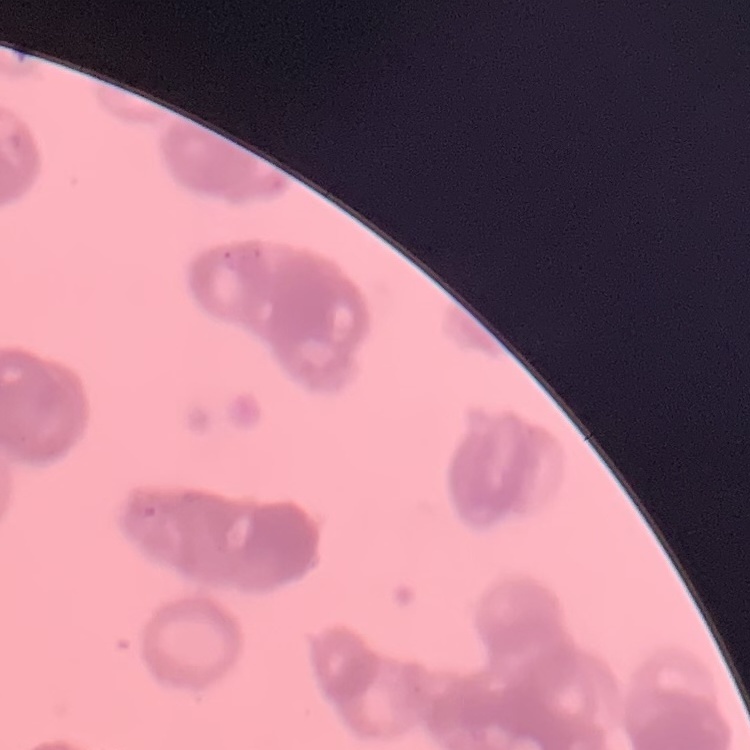
Summary:
  - Red blood cell morphology: rouleaux formation
  - Stain: Field's or Giemsa
  - Image type: square crop of a larger photomicrograph
  - Preparation: thin blood smear